Give the position of every leukocyte visible.
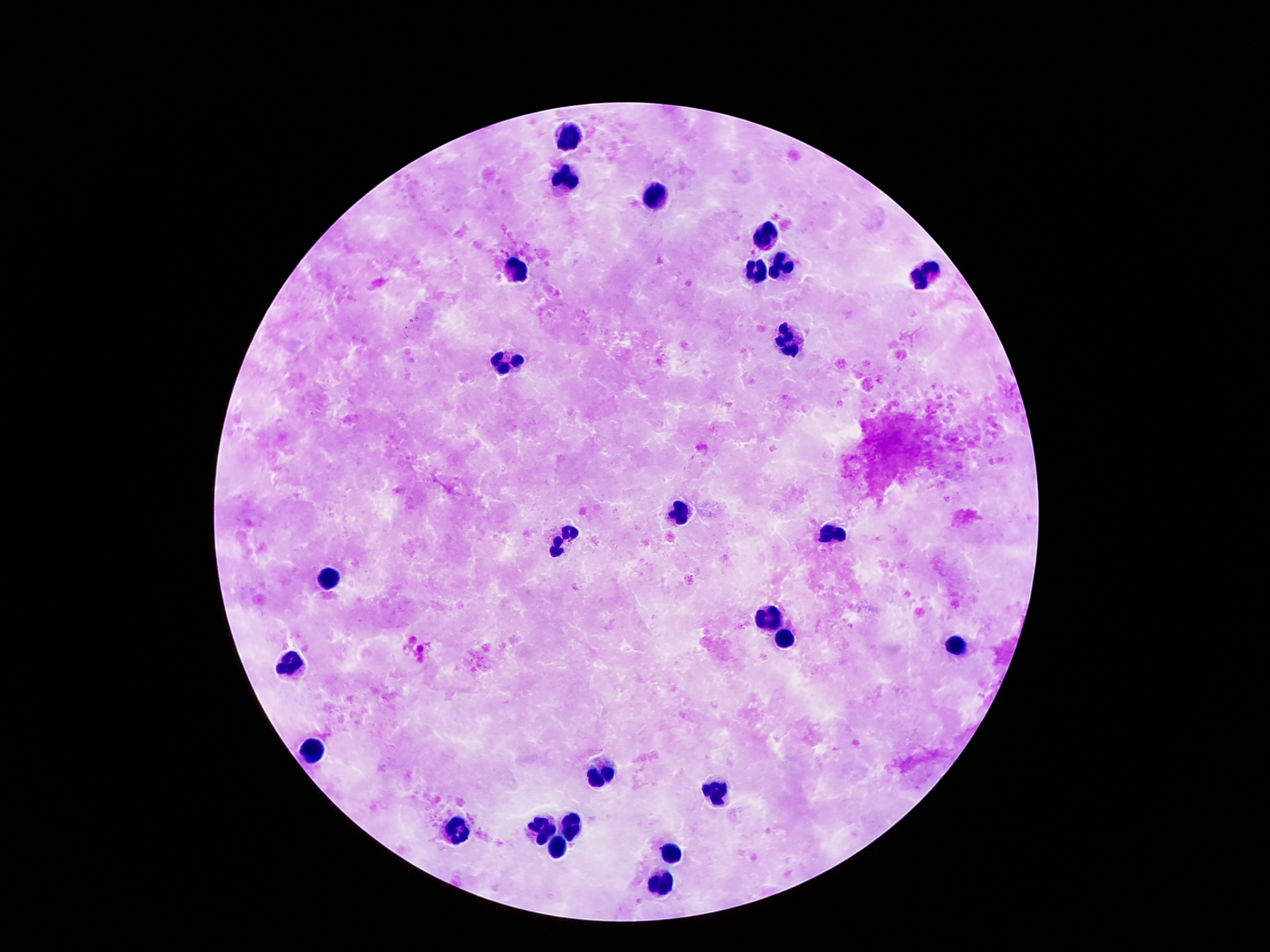
Approximate centers as (x, y) in pixels.
Leukocytes: (568, 135), (565, 182), (649, 200), (763, 241), (784, 267), (520, 268), (755, 273), (926, 274), (787, 342), (510, 361), (679, 512), (832, 532), (560, 541), (328, 581), (767, 619), (784, 643), (957, 648), (295, 660), (313, 753), (602, 772), (711, 794), (573, 826), (540, 828), (458, 830), (557, 851), (671, 856), (658, 883).

stain = Giemsa
magnification = 100x
image size = 1270×952 pixels
preparation = thick blood smear
patient malaria status = uninfected
field of view = single
capture = smartphone camera through the microscope eyepiece